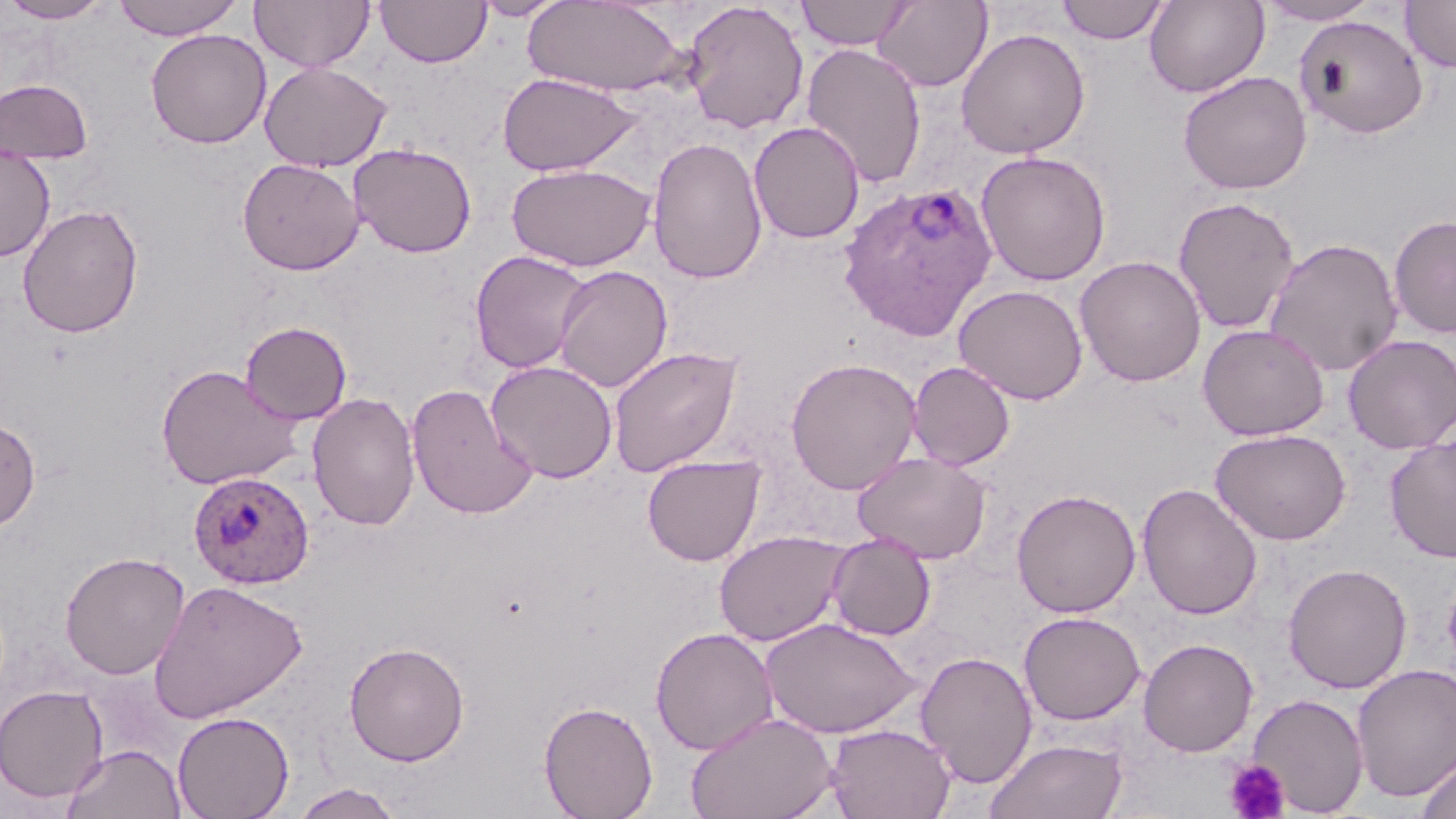

slide_level_diagnosis: Plasmodium ovale
field_of_view: single
modality: optical microscopy
platelet_locations: 'approximate bounding boxes as named x1/y1/x2/y2 corners in pixels: (x1=1224, y1=758, x2=1290, y2=819)'
uninfected_red_blood_cell_locations: 'approximate bounding boxes as named x1/y1/x2/y2 corners in pixels: (x1=0, y1=0, x2=113, y2=24), (x1=250, y1=0, x2=374, y2=72), (x1=375, y1=0, x2=492, y2=67), (x1=473, y1=0, x2=569, y2=21), (x1=794, y1=0, x2=915, y2=50), (x1=872, y1=0, x2=993, y2=92), (x1=1056, y1=0, x2=1170, y2=45), (x1=1144, y1=0, x2=1270, y2=97), (x1=1258, y1=0, x2=1381, y2=25), (x1=112, y1=1, x2=245, y2=40), (x1=523, y1=1, x2=690, y2=97), (x1=681, y1=1, x2=809, y2=135), (x1=1400, y1=1, x2=1456, y2=73), (x1=1294, y1=14, x2=1428, y2=139), (x1=146, y1=28, x2=271, y2=149), (x1=955, y1=28, x2=1090, y2=159), (x1=801, y1=42, x2=927, y2=188), (x1=259, y1=61, x2=392, y2=171), (x1=1178, y1=70, x2=1312, y2=195), (x1=497, y1=72, x2=640, y2=176), (x1=0, y1=78, x2=94, y2=165), (x1=748, y1=121, x2=865, y2=244), (x1=647, y1=136, x2=767, y2=284), (x1=349, y1=142, x2=477, y2=258), (x1=0, y1=146, x2=55, y2=262), (x1=975, y1=150, x2=1111, y2=285), (x1=237, y1=157, x2=364, y2=275), (x1=505, y1=162, x2=655, y2=272), (x1=1173, y1=196, x2=1299, y2=334), (x1=17, y1=204, x2=144, y2=338), (x1=1388, y1=214, x2=1456, y2=339), (x1=1264, y1=237, x2=1404, y2=377), (x1=469, y1=250, x2=593, y2=374), (x1=1075, y1=255, x2=1207, y2=387), (x1=553, y1=265, x2=672, y2=393), (x1=953, y1=284, x2=1088, y2=404), (x1=240, y1=321, x2=352, y2=424), (x1=1197, y1=323, x2=1330, y2=440), (x1=1342, y1=334, x2=1456, y2=454), (x1=608, y1=345, x2=743, y2=477), (x1=785, y1=357, x2=921, y2=494), (x1=486, y1=360, x2=618, y2=483), (x1=907, y1=361, x2=1015, y2=471), (x1=155, y1=363, x2=304, y2=490), (x1=406, y1=383, x2=539, y2=520), (x1=307, y1=392, x2=420, y2=530), (x1=0, y1=417, x2=41, y2=531), (x1=1210, y1=428, x2=1351, y2=545), (x1=1384, y1=435, x2=1456, y2=561), (x1=853, y1=451, x2=992, y2=564), (x1=641, y1=454, x2=766, y2=566), (x1=1137, y1=483, x2=1263, y2=620), (x1=1010, y1=488, x2=1141, y2=618), (x1=714, y1=530, x2=849, y2=646), (x1=826, y1=533, x2=936, y2=640), (x1=59, y1=550, x2=190, y2=680), (x1=1283, y1=562, x2=1413, y2=694), (x1=148, y1=579, x2=307, y2=724), (x1=1018, y1=611, x2=1146, y2=725), (x1=759, y1=617, x2=922, y2=739), (x1=1022, y1=621, x2=1262, y2=739), (x1=650, y1=627, x2=779, y2=755), (x1=1138, y1=638, x2=1259, y2=756), (x1=343, y1=641, x2=470, y2=766), (x1=915, y1=650, x2=1038, y2=789), (x1=1351, y1=663, x2=1456, y2=804), (x1=0, y1=683, x2=110, y2=803), (x1=1247, y1=693, x2=1368, y2=816), (x1=539, y1=700, x2=658, y2=819), (x1=172, y1=711, x2=294, y2=819), (x1=685, y1=711, x2=839, y2=819), (x1=824, y1=722, x2=957, y2=819), (x1=984, y1=737, x2=1129, y2=819), (x1=62, y1=743, x2=186, y2=819), (x1=1416, y1=749, x2=1456, y2=819), (x1=289, y1=783, x2=404, y2=819)'
preparation: thin blood smear
magnification: 1000x
stain: May-Grünwald-Giemsa
plasmodium_ovale_infected_red_blood_cell_locations: 'approximate bounding boxes as named x1/y1/x2/y2 corners in pixels: (x1=837, y1=181, x2=999, y2=340), (x1=188, y1=470, x2=315, y2=589)'
image_size: 1456×819 pixels